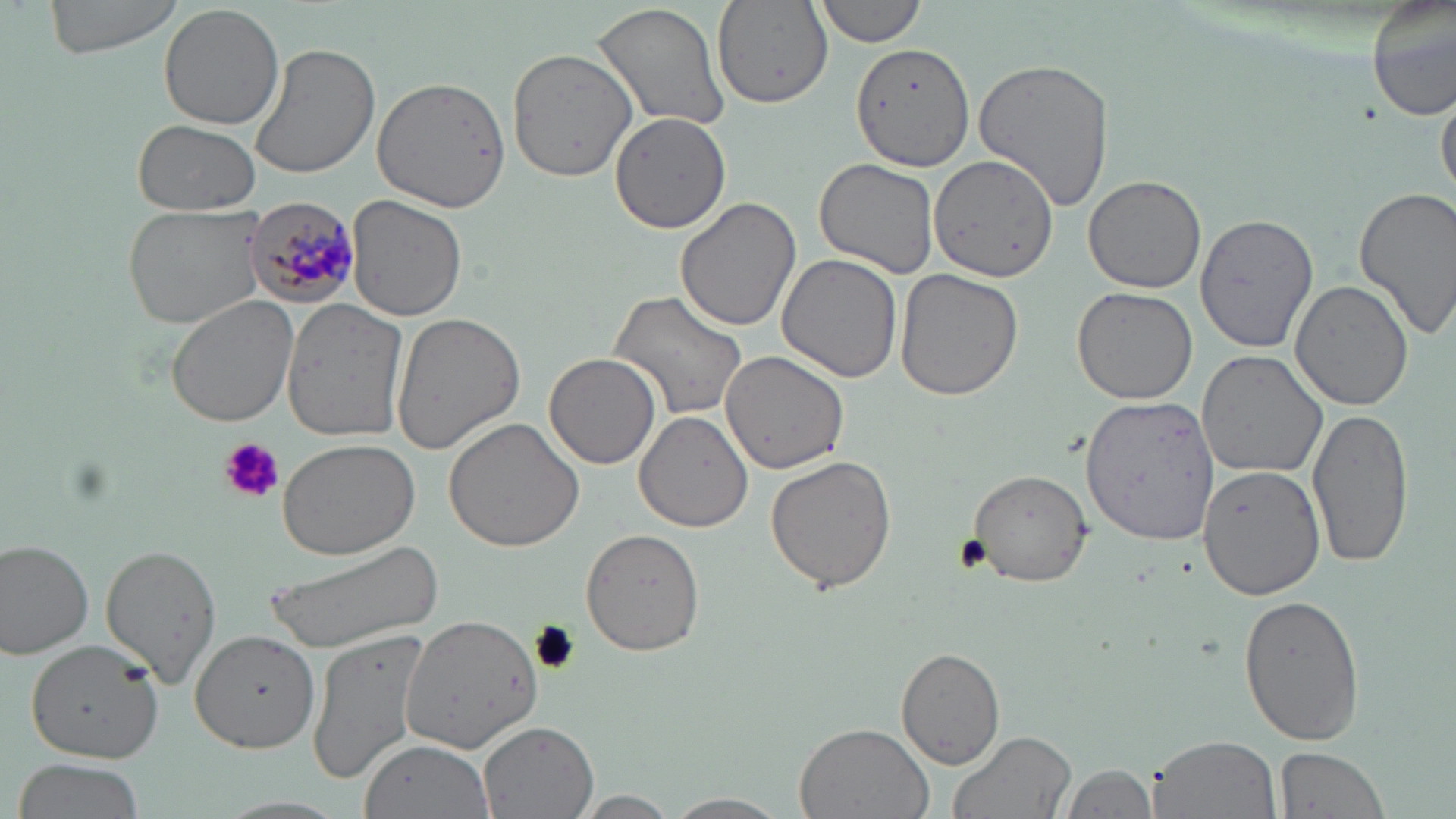
{
  "slide_level_diagnosis": "Plasmodium malariae",
  "uninfected_red_blood_cell_locations": "approximate bounding boxes as (x1, y1, x2, y2) in pixels: (40, 0, 192, 59), (1366, 0, 1455, 123), (591, 1, 732, 134), (712, 1, 833, 108), (813, 1, 926, 48), (158, 4, 284, 130), (850, 42, 974, 174), (508, 43, 650, 179), (250, 44, 380, 180), (973, 56, 1114, 214), (372, 75, 512, 212), (1437, 81, 1456, 204), (608, 112, 733, 235), (133, 119, 259, 216), (931, 132, 1082, 286), (814, 157, 940, 278), (1083, 174, 1206, 293), (1352, 186, 1456, 341), (346, 194, 466, 322), (673, 197, 804, 333), (124, 202, 269, 330), (1196, 209, 1319, 354), (777, 253, 904, 384), (894, 268, 1024, 401), (1290, 280, 1415, 411), (1071, 288, 1199, 404), (608, 289, 747, 420), (167, 294, 297, 427), (281, 299, 409, 441), (391, 313, 527, 454), (720, 350, 850, 474), (1196, 350, 1328, 479), (544, 355, 661, 469), (1083, 392, 1219, 546), (1308, 406, 1415, 567), (635, 411, 754, 533), (443, 415, 588, 552), (278, 438, 420, 559), (763, 454, 900, 594), (1200, 465, 1326, 598), (967, 469, 1096, 582), (581, 528, 705, 655), (267, 539, 443, 654), (0, 540, 95, 660), (99, 541, 223, 689), (1240, 594, 1366, 746), (399, 610, 543, 756), (306, 626, 433, 785), (190, 630, 320, 753), (27, 637, 162, 763), (895, 648, 1005, 770), (479, 721, 599, 818), (790, 723, 935, 819), (946, 728, 1077, 819), (1147, 733, 1279, 818), (360, 739, 493, 818), (1274, 746, 1390, 819), (11, 757, 149, 819), (1058, 762, 1157, 819), (573, 791, 682, 817), (664, 791, 791, 818), (211, 795, 353, 819)",
  "plasmodium_malariae_infected_red_blood_cell_locations": "approximate bounding boxes as (x1, y1, x2, y2) in pixels: (247, 195, 362, 306)",
  "image_size": "1456×819 pixels",
  "preparation": "thin blood smear",
  "field_of_view": "one of a larger specimen",
  "modality": "light microscopy",
  "magnification": "1000x",
  "stain": "May-Grünwald-Giemsa",
  "platelet_locations": "approximate bounding boxes as (x1, y1, x2, y2) in pixels: (220, 437, 283, 504)"
}